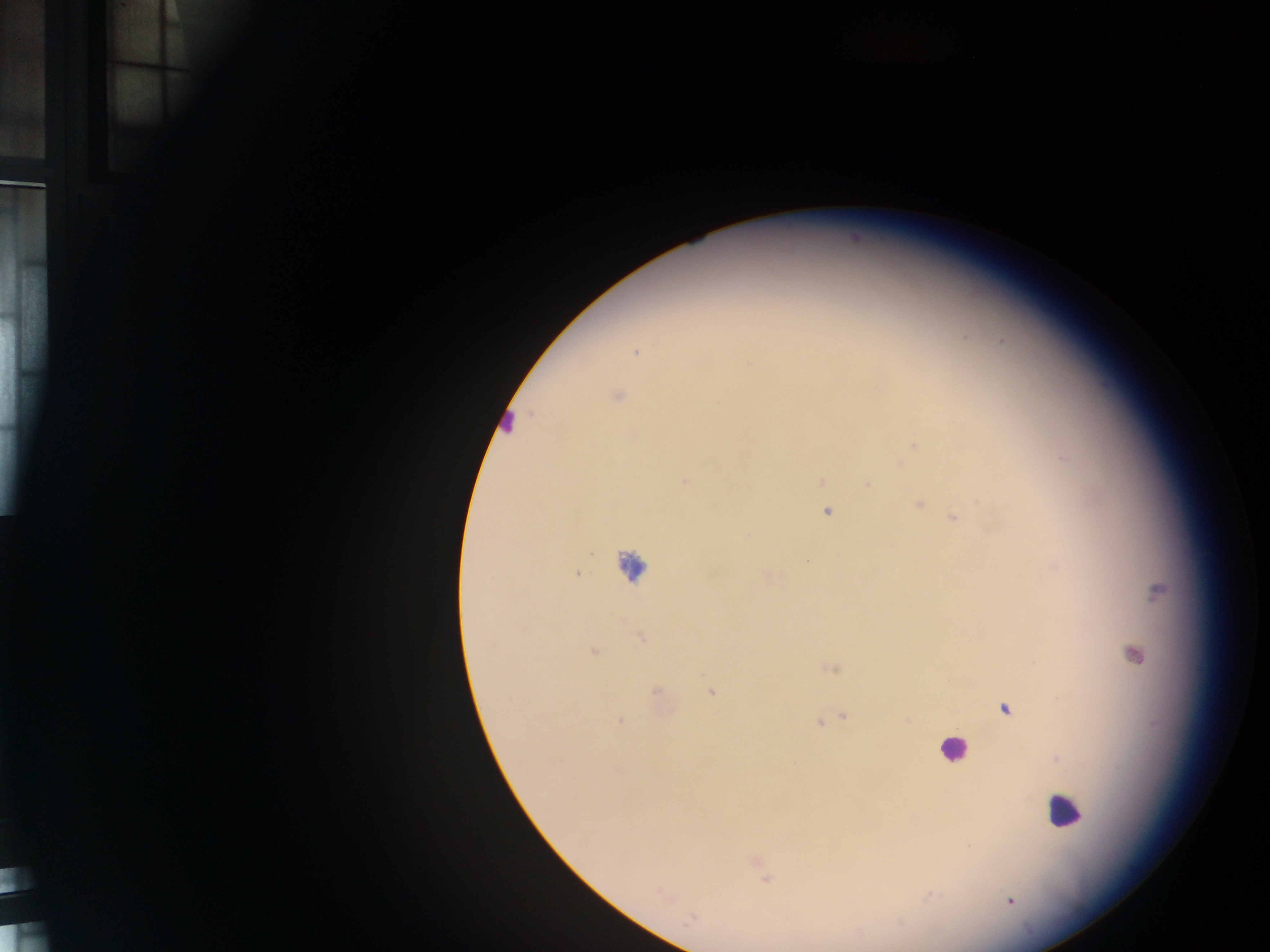 Approximate centers as [x, y] in pixels. Malaria parasite locations: [636, 353], [617, 396], [913, 445], [1061, 456], [899, 464], [684, 481], [820, 481], [867, 485], [918, 502], [827, 511], [953, 517], [1053, 566], [576, 573], [767, 576], [1157, 592], [641, 637], [593, 652], [830, 668], [710, 691], [657, 695], [1004, 708], [843, 717], [619, 720], [828, 720], [908, 720], [819, 723], [1056, 758], [758, 865], [765, 876], [929, 895], [1010, 901]. Leukocyte locations: [507, 423], [629, 565], [1137, 654], [952, 750], [1064, 811]. One field of view. Image is 1270×952 pixels. Sample from Ghana. Thick blood smear. Photographed through a microscope with a mobile-phone camera.